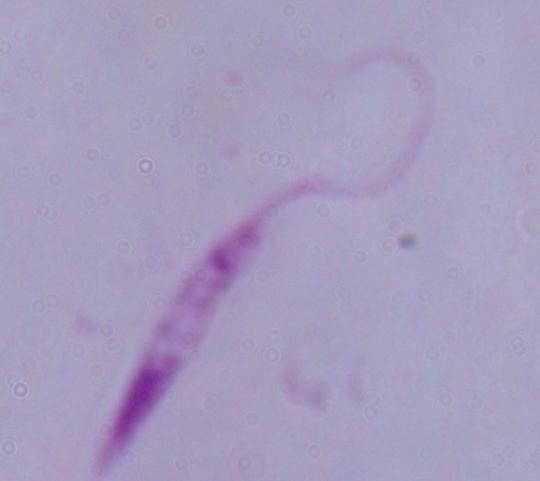
Summary:
  - Modality: photomicrograph
  - Identification: Leishmania
  - Magnification: 1000x